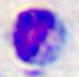 400x magnification. Photomicrograph. A white blood cell is shown.